State which parasite is depicted.
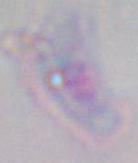

This is Toxoplasma gondii.

Captured at 1000x magnification. Micrograph.